Assess this cell for malaria.
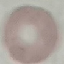

Uninfected.

{
  "image_type": "automatically extracted cell patch, resized to 64 × 64 pixels",
  "preparation": "thin blood smear",
  "capture": "smartphone camera at the microscope eyepiece",
  "stain": "Giemsa"
}